Report the malaria status of this cell.
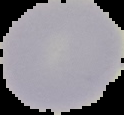
Uninfected.

image size = 124×115 pixels
image type = segmented cell region on a black background
preparation = thin blood film